Outline each Plasmodium ovale-infected red blood cell.
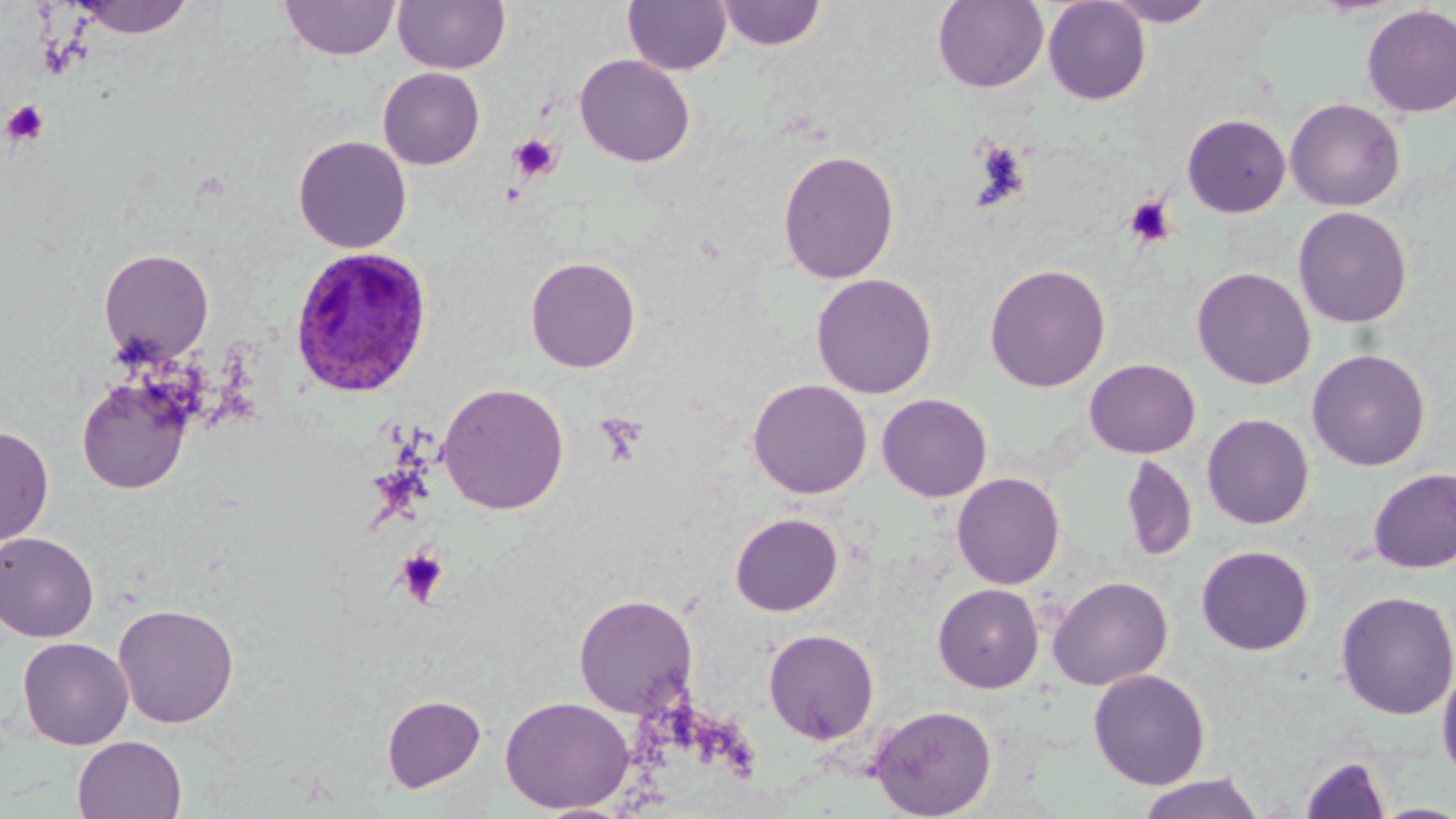

Approximate bounding boxes as (x1, y1, x2, y2) in pixels.
Plasmodium ovale-infected red blood cells: (287, 245, 436, 399).

Platelet locations: (2, 99, 50, 147), (508, 132, 563, 183), (973, 141, 1031, 208), (1124, 196, 1176, 248), (594, 413, 649, 467), (394, 547, 449, 607). Uninfected red blood cell locations: (73, 0, 198, 39), (279, 0, 401, 61), (393, 0, 510, 74), (622, 0, 732, 75), (1042, 0, 1151, 105), (1102, 0, 1220, 27), (716, 1, 826, 51), (932, 1, 1049, 92), (1360, 4, 1456, 118), (574, 54, 695, 167), (377, 67, 486, 170), (1285, 98, 1405, 212), (1181, 113, 1291, 218), (293, 135, 412, 253), (777, 148, 900, 284), (1292, 206, 1413, 329), (99, 248, 214, 363), (524, 255, 641, 373), (984, 262, 1111, 393), (1191, 266, 1316, 390), (811, 273, 938, 398), (1306, 348, 1430, 471), (1084, 358, 1200, 458), (76, 374, 194, 495), (747, 378, 872, 499), (437, 382, 570, 515), (876, 393, 992, 502), (1201, 412, 1314, 529), (0, 425, 54, 547), (1120, 455, 1197, 562), (1367, 467, 1456, 573), (951, 472, 1066, 589), (729, 512, 843, 616), (0, 531, 99, 642), (1195, 545, 1315, 655), (1048, 575, 1173, 690), (932, 583, 1044, 693), (1334, 589, 1456, 720), (573, 594, 698, 718), (112, 603, 240, 728), (763, 628, 879, 745), (17, 637, 134, 749), (1436, 664, 1456, 784), (1087, 668, 1211, 790), (381, 694, 486, 792), (499, 696, 633, 814), (869, 704, 997, 819), (72, 735, 188, 819), (1299, 755, 1391, 818), (1134, 772, 1266, 819), (1370, 802, 1456, 819), (532, 803, 636, 819). Slide-level diagnosis: Plasmodium ovale. Thin blood film. Captured at 1000x magnification. Image is 1456×819 pixels. Light microscopy. May-Grünwald-Giemsa stain. One field of a larger specimen.